Give the location of every WBC.
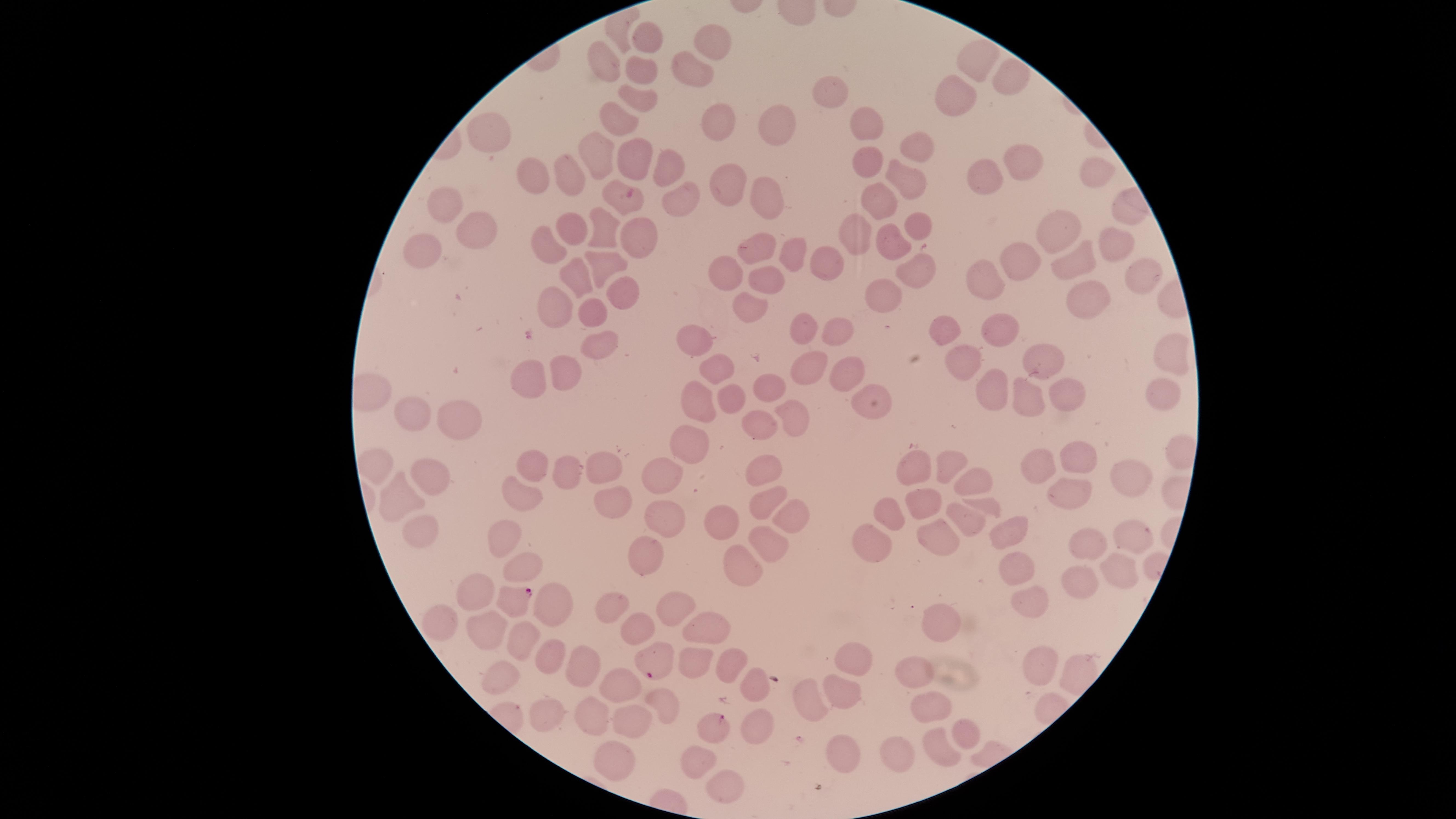
No WBCs identified.

Approximate marker points as (x, y) in pixels.
Summary:
  - Uninfected RBCs: (644, 37), (722, 42), (610, 56), (976, 58), (693, 69), (641, 73), (1004, 77), (835, 91), (641, 99), (956, 99), (718, 115), (620, 118), (867, 124), (772, 126), (492, 135), (920, 148), (602, 154), (868, 158), (1016, 158), (631, 164), (659, 170), (984, 174), (911, 177), (539, 178), (1098, 178), (569, 180), (736, 182), (765, 192), (683, 193), (631, 197), (879, 198), (447, 207), (860, 224), (1062, 224), (576, 229), (916, 229), (608, 231), (476, 233), (641, 234), (1113, 244), (760, 246), (896, 246), (553, 250), (793, 251), (427, 255), (1084, 255), (830, 259), (603, 263), (1031, 263), (914, 267), (728, 271), (579, 277), (1142, 277), (765, 279), (993, 281), (621, 295), (887, 296), (1082, 296), (555, 304), (749, 305), (592, 311), (952, 328), (1000, 328), (808, 331), (838, 332), (599, 340), (693, 344), (1167, 353), (969, 363), (1045, 363), (811, 368), (712, 370), (845, 370), (564, 374), (529, 377), (774, 384), (993, 387), (730, 390), (1067, 394), (1170, 394), (699, 395), (866, 396), (1024, 397), (417, 410), (455, 415), (790, 417), (756, 419), (690, 442), (1080, 458), (380, 462), (531, 464), (948, 466), (1041, 466), (599, 469), (569, 470), (660, 470), (912, 471), (764, 472), (1128, 474), (427, 476), (970, 486), (520, 491), (764, 493), (1064, 494), (405, 498), (611, 501), (923, 505), (982, 505), (788, 513), (892, 516), (660, 523), (964, 523), (719, 528), (1004, 530), (502, 533), (416, 535), (935, 535), (1090, 538), (1126, 539), (771, 540), (867, 542), (636, 556), (516, 562), (741, 563), (1120, 565), (1011, 566), (1077, 579), (472, 591), (1026, 596), (548, 601), (611, 606), (670, 606), (445, 620), (630, 624), (944, 625), (706, 628), (482, 632), (516, 638), (554, 652), (852, 658), (727, 660), (693, 662), (1048, 664), (584, 670), (915, 676), (499, 677), (748, 682), (617, 687), (804, 699), (832, 700), (657, 704), (925, 709), (544, 714), (593, 714), (629, 724), (756, 725), (958, 729), (936, 748), (838, 751), (889, 755), (697, 756), (611, 760), (726, 775)
  - Parasitized RBCs: (513, 600), (657, 663), (716, 724)
  - Presence: malaria parasites seen
  - Visible region: circular
  - Image size: 1456×819 pixels
  - Field of view: single
  - Preparation: thin blood smear
  - Capture: smartphone photograph through the microscope eyepiece
  - Species: Plasmodium falciparum
  - Stain: Giemsa